Describe the morphology of the red blood cells.
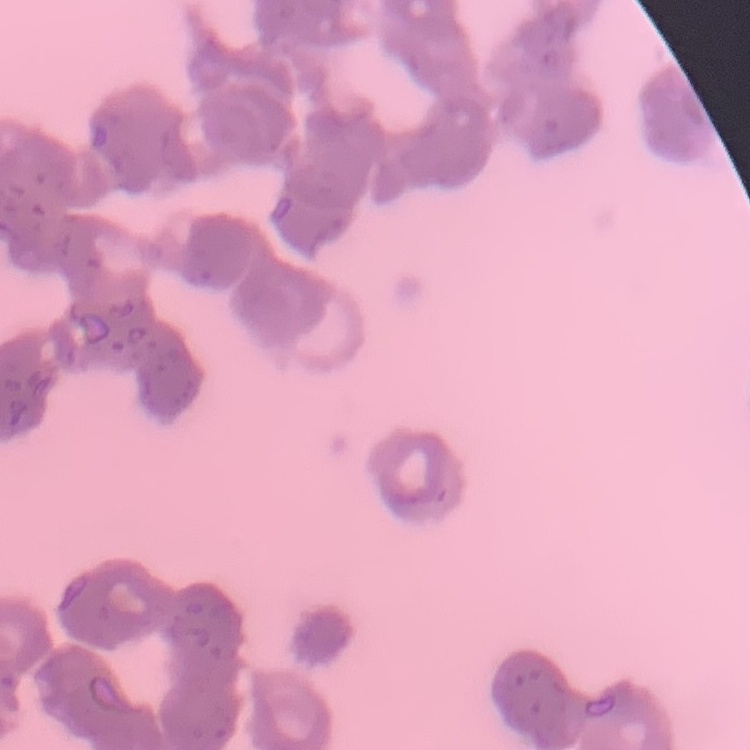

They show rouleaux formation.

Summary:
  - Image type: one tile cut from a larger photomicrograph
  - Stain: Field's or Giemsa
  - Preparation: thin blood film